State the blood parasite species.
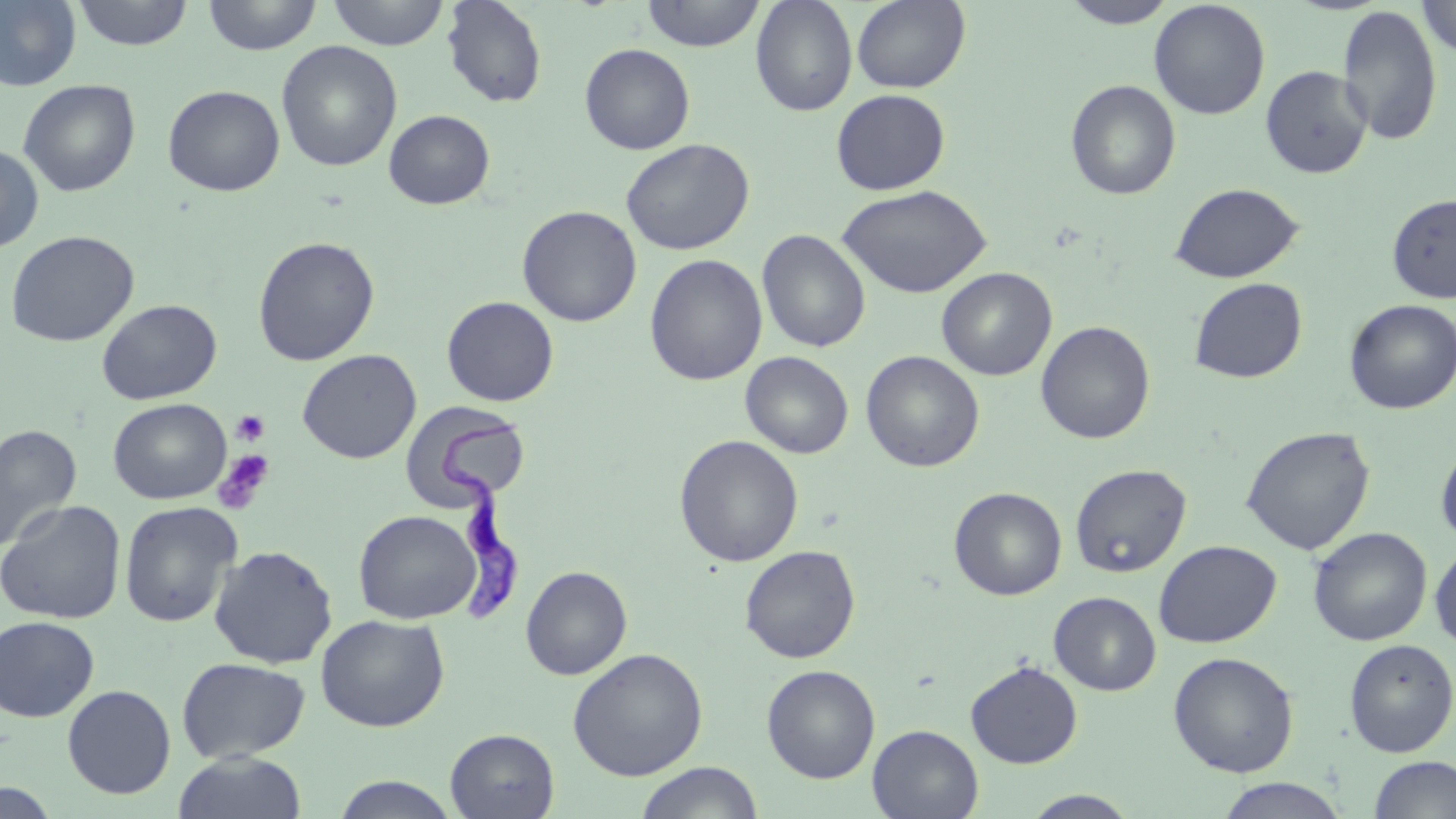

Trypanosoma brucei.

Summary:
  - Coordinate format: approximate bounding boxes as named x1/y1/x2/y2 corners in pixels
  - Trypanosoma brucei locations: (x1=433, y1=408, x2=525, y2=626)
  - Platelet locations: (x1=231, y1=409, x2=271, y2=447), (x1=213, y1=449, x2=276, y2=514)
  - Uninfected red blood cell locations: (x1=0, y1=0, x2=82, y2=91), (x1=71, y1=0, x2=195, y2=50), (x1=202, y1=0, x2=323, y2=55), (x1=325, y1=0, x2=450, y2=50), (x1=441, y1=0, x2=548, y2=108), (x1=641, y1=0, x2=766, y2=51), (x1=750, y1=0, x2=858, y2=116), (x1=851, y1=0, x2=971, y2=93), (x1=1417, y1=0, x2=1456, y2=59), (x1=1060, y1=1, x2=1178, y2=28), (x1=1148, y1=1, x2=1271, y2=120), (x1=1337, y1=5, x2=1443, y2=146), (x1=276, y1=41, x2=402, y2=171), (x1=579, y1=43, x2=695, y2=155), (x1=1260, y1=65, x2=1373, y2=179), (x1=18, y1=79, x2=141, y2=197), (x1=1065, y1=79, x2=1181, y2=200), (x1=162, y1=84, x2=285, y2=196), (x1=831, y1=88, x2=950, y2=195), (x1=384, y1=109, x2=495, y2=209), (x1=620, y1=138, x2=755, y2=256), (x1=0, y1=143, x2=45, y2=253), (x1=1169, y1=183, x2=1304, y2=284), (x1=837, y1=184, x2=991, y2=298), (x1=1386, y1=194, x2=1456, y2=303), (x1=517, y1=205, x2=642, y2=327), (x1=757, y1=229, x2=871, y2=353), (x1=5, y1=230, x2=140, y2=347), (x1=252, y1=236, x2=380, y2=366), (x1=644, y1=253, x2=767, y2=386), (x1=937, y1=267, x2=1057, y2=381), (x1=1189, y1=277, x2=1308, y2=384), (x1=442, y1=296, x2=559, y2=406), (x1=96, y1=299, x2=222, y2=404), (x1=1344, y1=299, x2=1456, y2=414), (x1=1036, y1=321, x2=1155, y2=444), (x1=297, y1=349, x2=421, y2=464), (x1=741, y1=351, x2=853, y2=458), (x1=861, y1=351, x2=984, y2=472), (x1=107, y1=398, x2=232, y2=504), (x1=401, y1=401, x2=531, y2=511), (x1=1, y1=423, x2=80, y2=553), (x1=1240, y1=426, x2=1375, y2=555), (x1=674, y1=434, x2=804, y2=567), (x1=1435, y1=440, x2=1456, y2=548), (x1=1070, y1=463, x2=1191, y2=578), (x1=948, y1=486, x2=1067, y2=600), (x1=0, y1=499, x2=126, y2=624), (x1=119, y1=500, x2=242, y2=628), (x1=353, y1=509, x2=481, y2=624), (x1=1308, y1=527, x2=1432, y2=646), (x1=1153, y1=540, x2=1281, y2=648), (x1=208, y1=544, x2=338, y2=669), (x1=740, y1=545, x2=861, y2=663), (x1=1429, y1=545, x2=1456, y2=651), (x1=520, y1=565, x2=632, y2=680), (x1=1049, y1=591, x2=1161, y2=695), (x1=315, y1=614, x2=450, y2=732), (x1=0, y1=615, x2=99, y2=721), (x1=1344, y1=638, x2=1456, y2=757), (x1=567, y1=647, x2=708, y2=781), (x1=1167, y1=651, x2=1299, y2=777), (x1=176, y1=657, x2=311, y2=762), (x1=965, y1=661, x2=1082, y2=768), (x1=761, y1=664, x2=881, y2=783), (x1=62, y1=684, x2=176, y2=799), (x1=867, y1=724, x2=984, y2=818), (x1=445, y1=728, x2=560, y2=818), (x1=172, y1=751, x2=308, y2=819), (x1=1368, y1=756, x2=1456, y2=818), (x1=634, y1=762, x2=764, y2=819), (x1=329, y1=775, x2=461, y2=818), (x1=1215, y1=778, x2=1349, y2=818), (x1=0, y1=781, x2=63, y2=819), (x1=1021, y1=790, x2=1142, y2=818)
  - Stain: May-Grünwald-Giemsa
  - Modality: light microscopy
  - Image size: 1456×819 pixels
  - Preparation: thin blood film
  - Field of view: one of a larger specimen
  - Magnification: 1000x